Assess this cell for malaria.
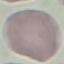

Uninfected.

{
  "preparation": "thin blood film",
  "image_type": "automatically extracted cell patch, resized to 64 × 64 pixels",
  "stain": "Giemsa",
  "capture": "smartphone through the microscope eyepiece"
}